Locate every Plasmodium parasite.
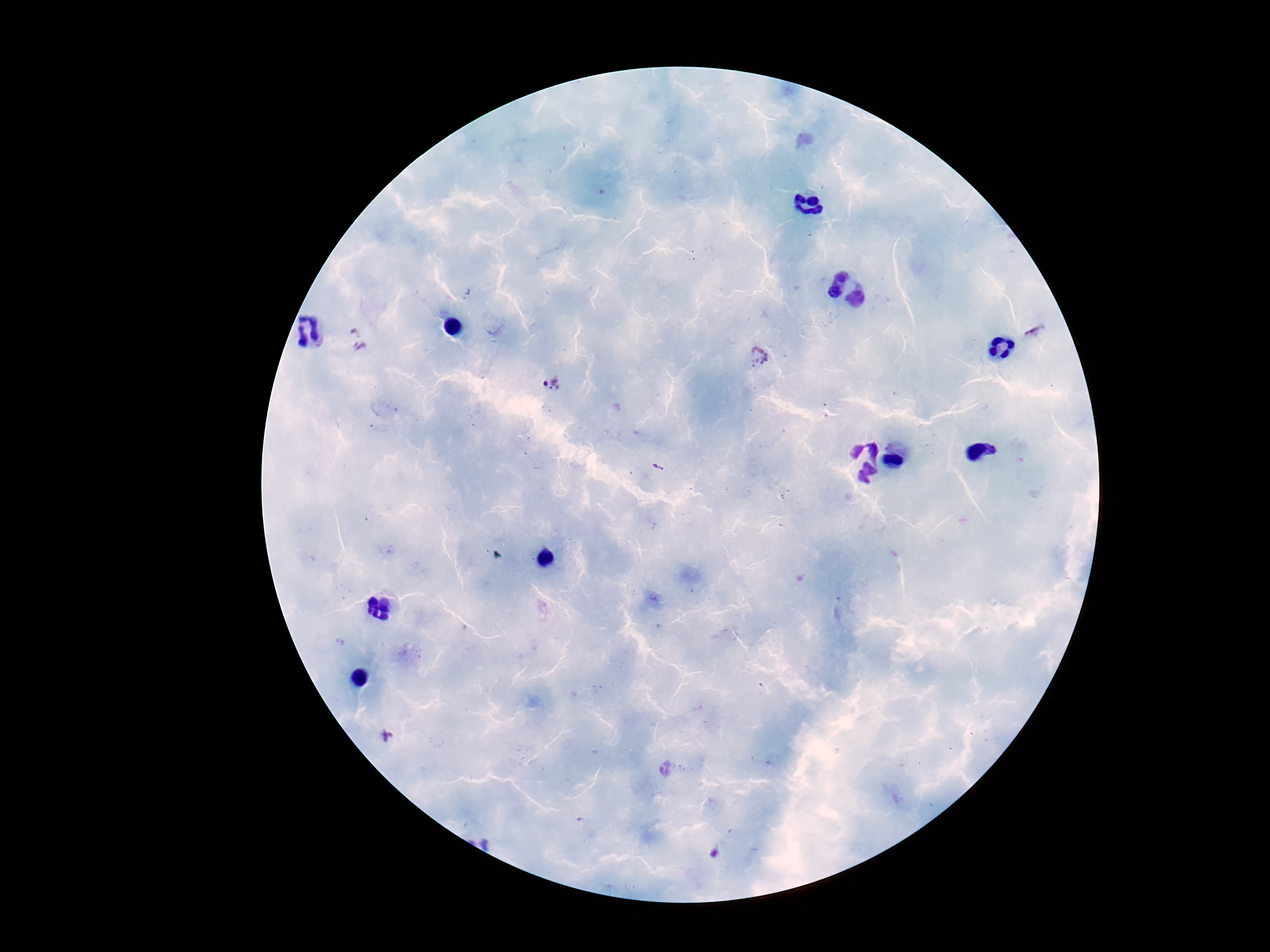

Approximate centers as {x, y} in pixels.
Plasmodium parasites: {357, 337}, {759, 359}, {553, 384}, {387, 736}, {717, 853}.

100x magnification. Giemsa-stained preparation. Thick peripheral-blood smear. Patient malaria status: positive. Single field of view. Image is 1270×952 pixels. Smartphone photograph taken through the microscope eyepiece.